Assess for malaria.
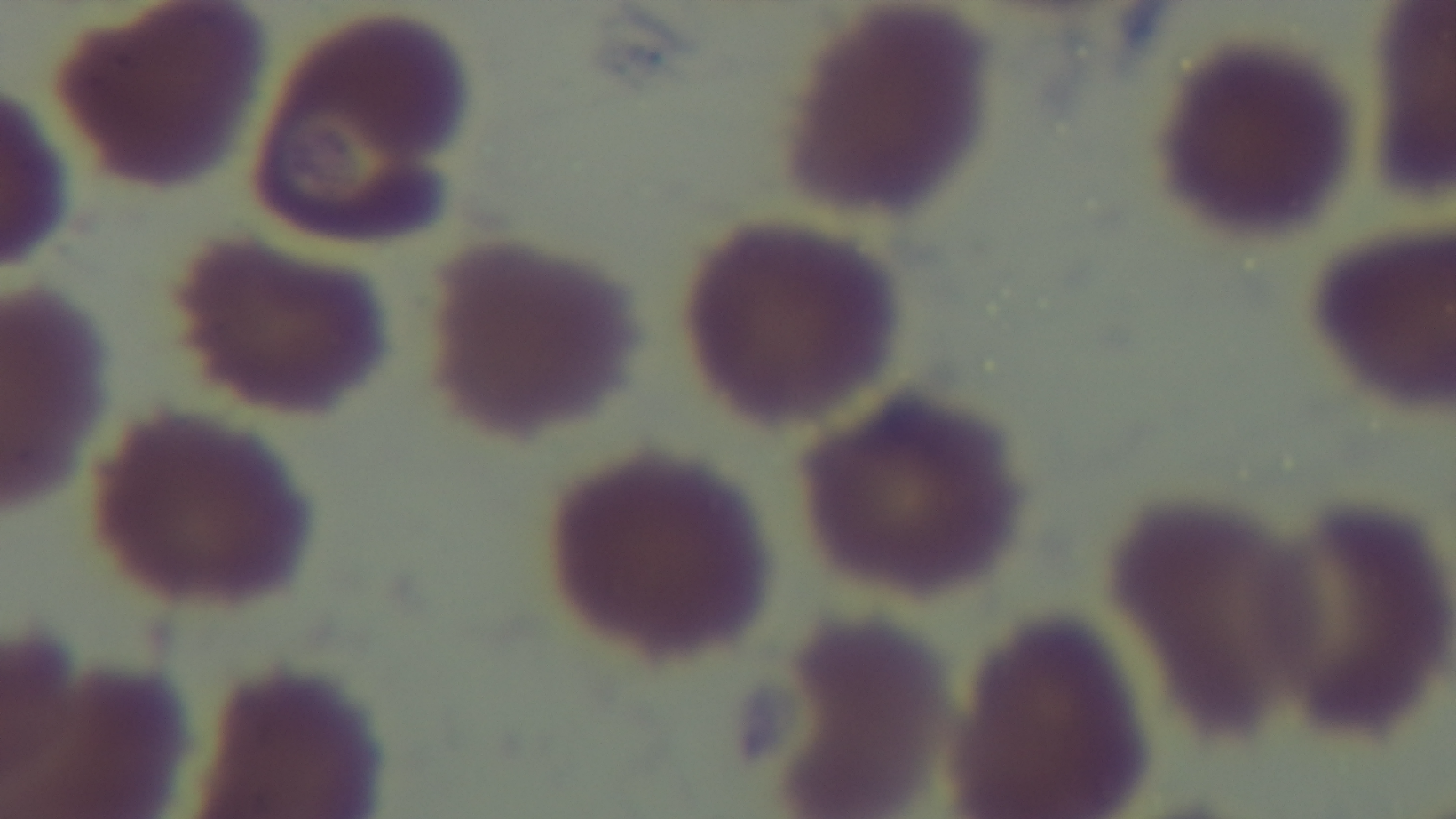

Uninfected.

Summary:
  - Stain: Giemsa
  - Capture: mounted 4K digital camera
  - Preparation: thin
  - Modality: light microscopy
  - Field of view: one from the slide
  - Objective: 100x oil immersion